Outline each white blood cell.
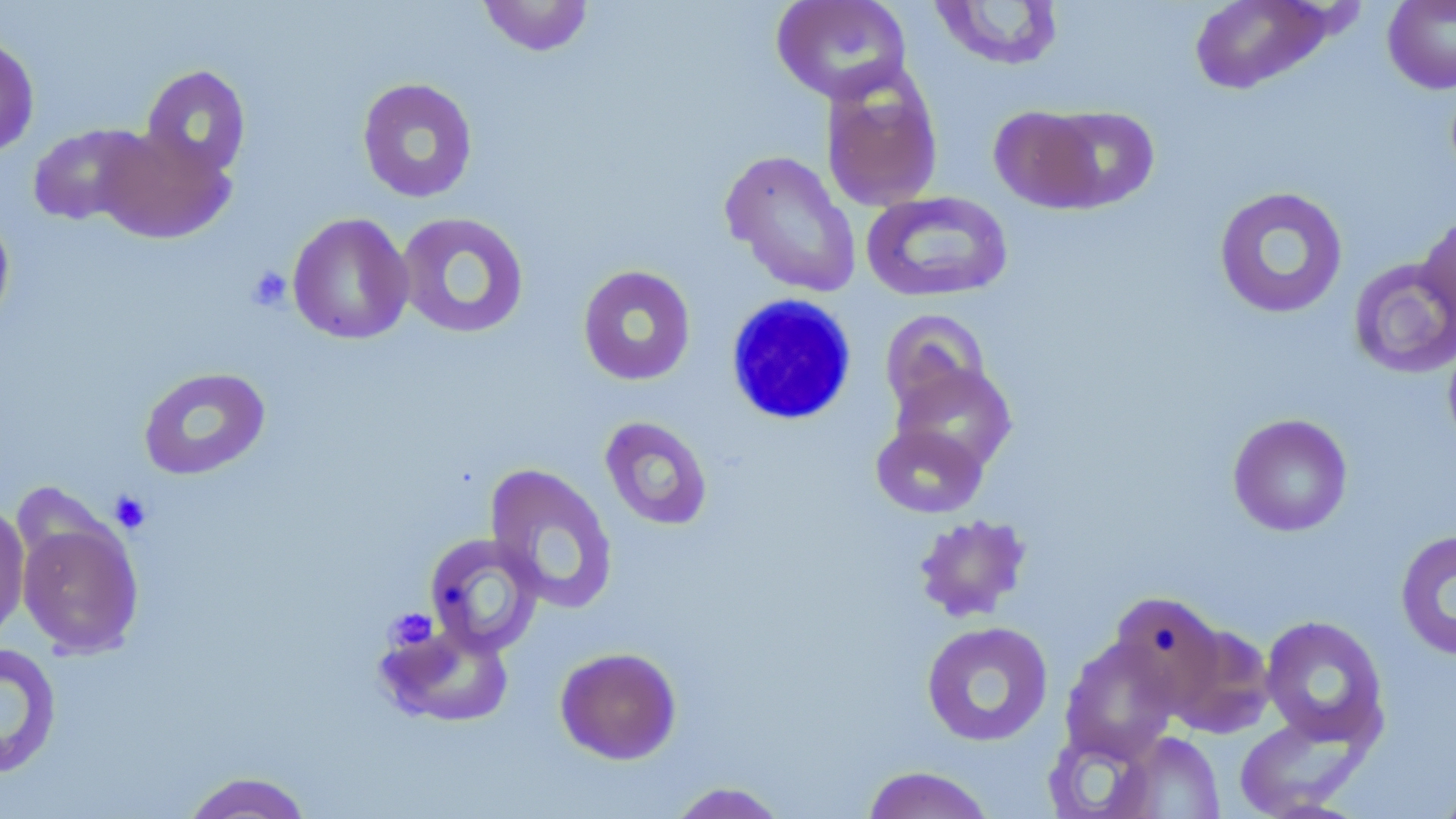
Approximate bounding boxes as [x1, y1, x2, y2] in pixels.
White blood cells: [724, 294, 858, 427].

Summary:
  - Uninfected red blood cell locations: [477, 0, 595, 57], [770, 0, 913, 104], [1188, 0, 1334, 95], [1382, 0, 1456, 94], [928, 1, 1065, 72], [0, 34, 39, 159], [141, 65, 251, 179], [820, 67, 943, 212], [357, 77, 478, 203], [989, 105, 1106, 213], [1041, 106, 1160, 210], [27, 124, 149, 226], [95, 125, 234, 245], [721, 150, 861, 298], [1213, 186, 1349, 319], [861, 191, 1013, 303], [0, 209, 15, 332], [1416, 210, 1456, 327], [395, 212, 530, 340], [287, 213, 414, 345], [1348, 258, 1456, 378], [577, 264, 696, 386], [880, 309, 992, 416], [1442, 333, 1456, 455], [890, 361, 1017, 475], [137, 366, 271, 481], [1227, 413, 1353, 537], [600, 416, 713, 531], [870, 420, 989, 519], [484, 463, 619, 613], [0, 500, 31, 647], [913, 513, 1032, 623], [16, 514, 144, 658], [1395, 529, 1456, 661], [423, 532, 545, 656], [1109, 591, 1227, 708], [1260, 615, 1389, 748], [378, 620, 515, 728], [920, 621, 1054, 747], [1167, 622, 1275, 738], [1060, 637, 1180, 764], [0, 643, 62, 779], [554, 646, 682, 765], [1234, 714, 1369, 818], [1041, 726, 1160, 818], [1110, 730, 1225, 818], [861, 765, 997, 819], [179, 771, 315, 819], [1434, 776, 1456, 819], [665, 781, 790, 818]
  - Platelet locations: [247, 265, 292, 312], [109, 490, 152, 533], [386, 607, 438, 652]
  - Slide-level diagnosis: negative for blood parasites
  - Modality: optical microscopy
  - Image size: 1456×819 pixels
  - Magnification: 1000x
  - Field of view: single
  - Stain: May-Grünwald-Giemsa
  - Preparation: thin blood film